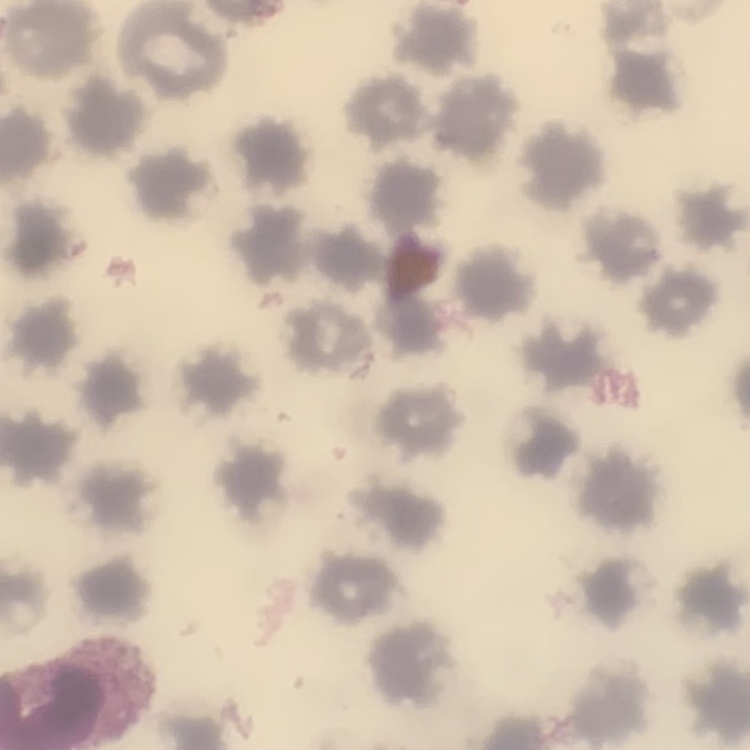

Summary:
  - Erythrocyte morphology: no rouleaux formation
  - Preparation: thin peripheral smear
  - Image type: one tile cut from a larger photomicrograph
  - Stain: Field's or Giemsa